State which parasite is depicted.
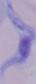
This is a trypanosome.

Photomicrograph. 1000x magnification.